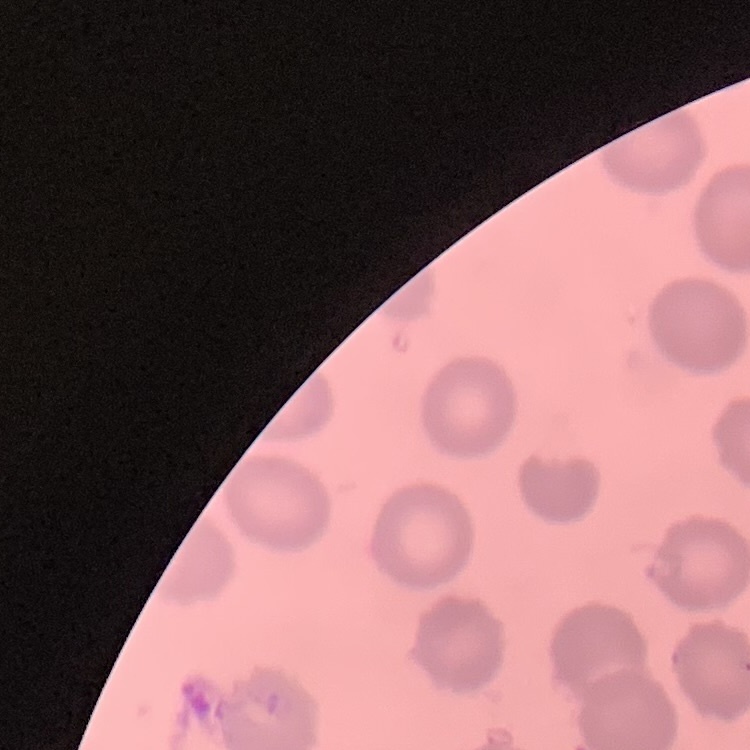

red blood cell morphology = no rouleaux formation
stain = Field's or Giemsa
preparation = thin peripheral smear
image type = square crop of a larger photomicrograph